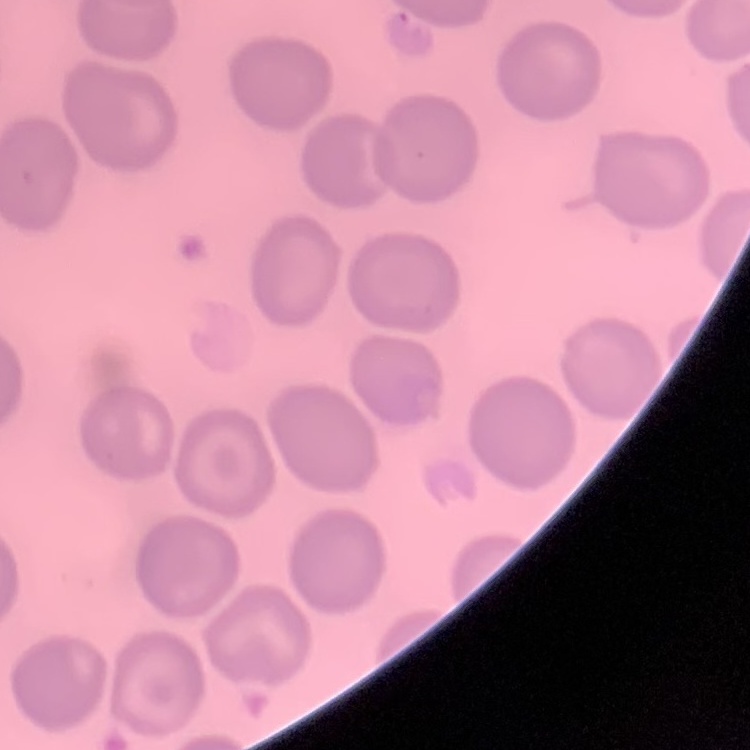
erythrocyte morphology = no rouleaux formation
stain = Field's or Giemsa
preparation = thin blood film
image type = one tile cut from a larger photomicrograph